Comment on the morphology of the red blood cells.
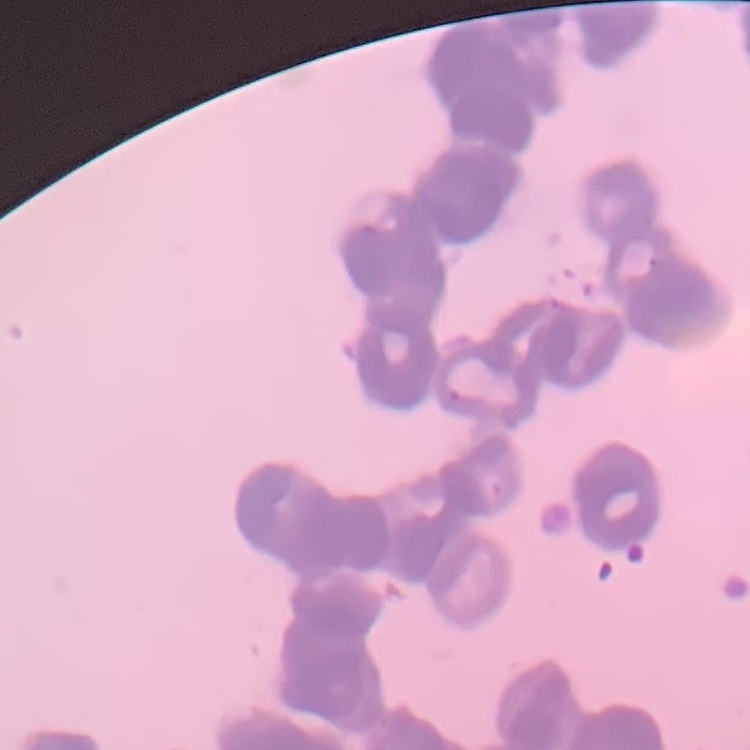

They show rouleaux formation.

preparation: thin blood film
stain: Field's or Giemsa
image_type: one tile cut from a larger photomicrograph